Assess the morphology of the erythrocytes.
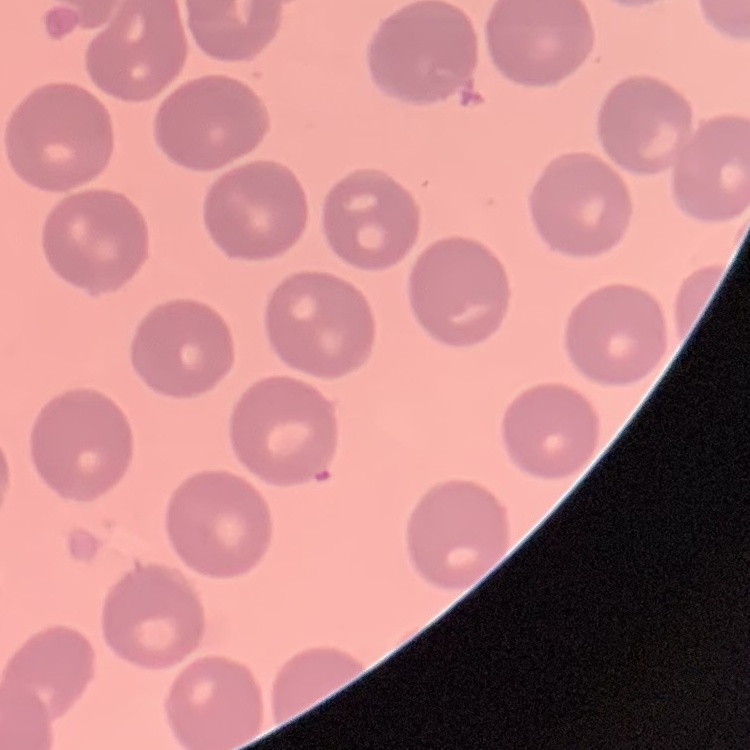
No rouleaux formation.

preparation = thin blood smear
image type = one tile cut from a larger photomicrograph
stain = Field's or Giemsa